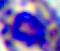
Summary:
  - Modality: micrograph
  - Identification: white blood cell
  - Magnification: 400x